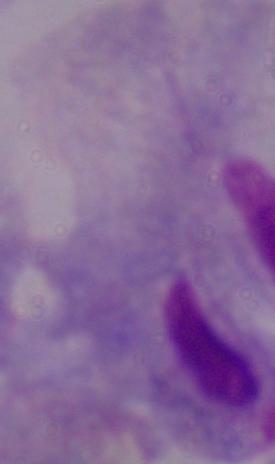 Captured at 1000x magnification. Micrograph. A trichomonad is shown.